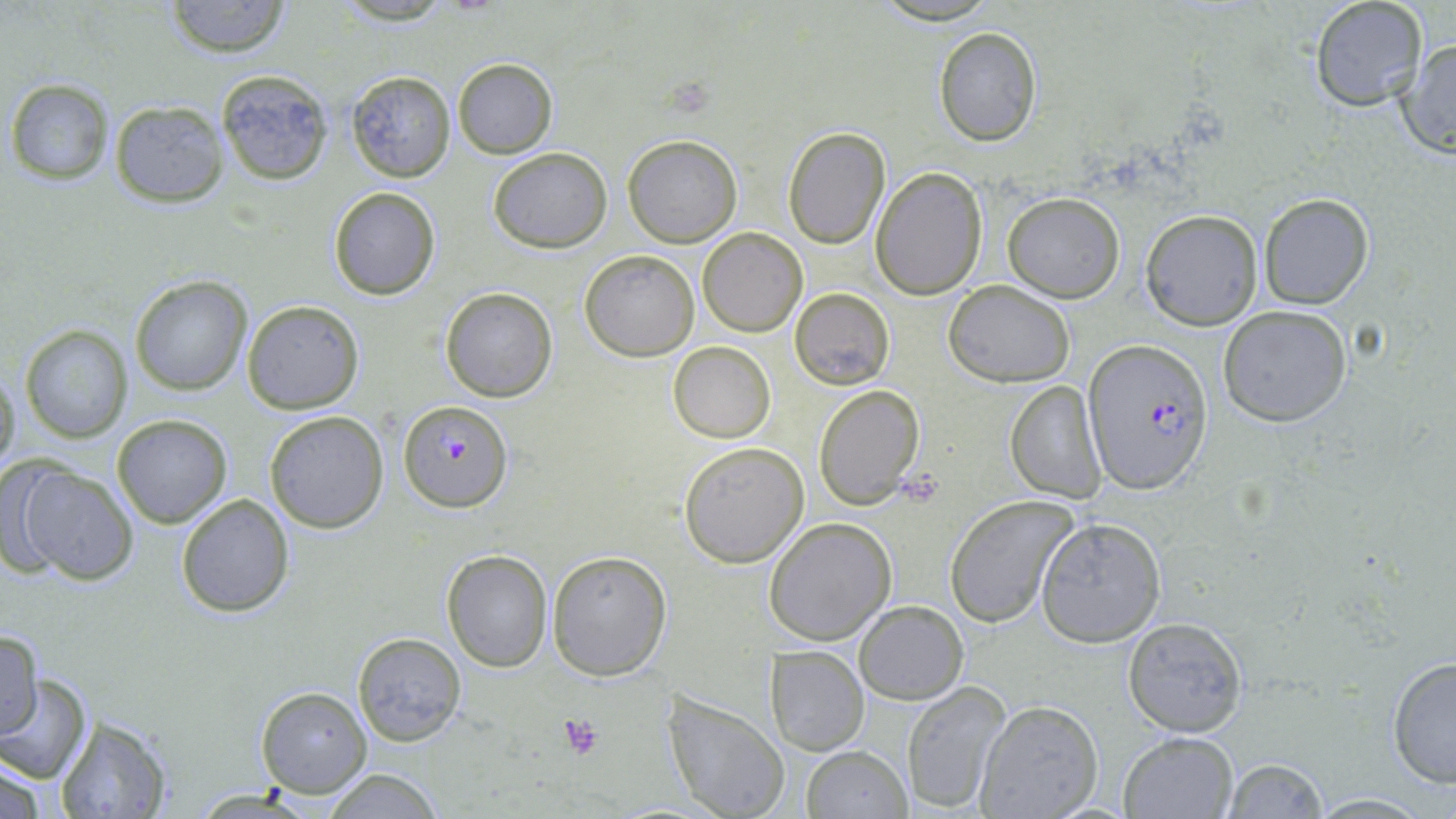

Approximate bounding boxes as (x1,y1)-(x2,y2) corner pairs in pixels. Uninfected red blood cell locations: (162,0)-(293,57), (1308,0)-(1429,112), (933,26)-(1043,146), (1397,37)-(1456,159), (452,57)-(558,158), (217,70)-(333,185), (347,70)-(456,183), (4,77)-(115,185), (108,100)-(228,207), (781,127)-(891,249), (623,133)-(742,247), (487,146)-(613,254), (871,167)-(989,300), (328,186)-(441,300), (1003,192)-(1125,303), (1258,193)-(1375,310), (1140,209)-(1263,330), (698,227)-(808,337), (580,250)-(699,361), (129,275)-(253,394), (943,280)-(1075,386), (440,286)-(559,403), (790,288)-(896,389), (241,299)-(364,414), (1217,305)-(1353,426), (21,324)-(132,443), (668,341)-(776,441), (0,364)-(22,484), (1004,379)-(1108,502), (813,383)-(924,512), (263,410)-(389,534), (111,414)-(233,529), (678,441)-(809,568), (13,464)-(139,585), (175,493)-(296,617), (943,496)-(1077,627), (1035,516)-(1166,647), (763,518)-(897,646), (441,548)-(554,672), (548,551)-(672,678), (854,601)-(968,704), (1122,616)-(1249,738), (2,627)-(44,738), (352,631)-(468,745), (765,646)-(869,755), (1385,654)-(1455,789), (0,672)-(94,785), (900,679)-(1012,814), (255,686)-(371,798), (662,693)-(789,819), (973,699)-(1105,819), (54,715)-(175,819), (1118,731)-(1238,817), (801,745)-(912,818), (0,754)-(55,819), (1222,757)-(1330,819), (319,767)-(448,819), (1305,793)-(1439,817). Platelet locations: (898,470)-(946,508), (557,715)-(604,759). Plasmodium falciparum-infected red blood cell locations: (1082,337)-(1215,495), (398,399)-(512,512). Slide-level diagnosis: Plasmodium falciparum. Thin blood smear. Captured at 1000x magnification. May-Grünwald-Giemsa-stained preparation. One field of a larger specimen. Image is 1456×819 pixels. Optical microscopy.